Assess the morphology of the red blood cells.
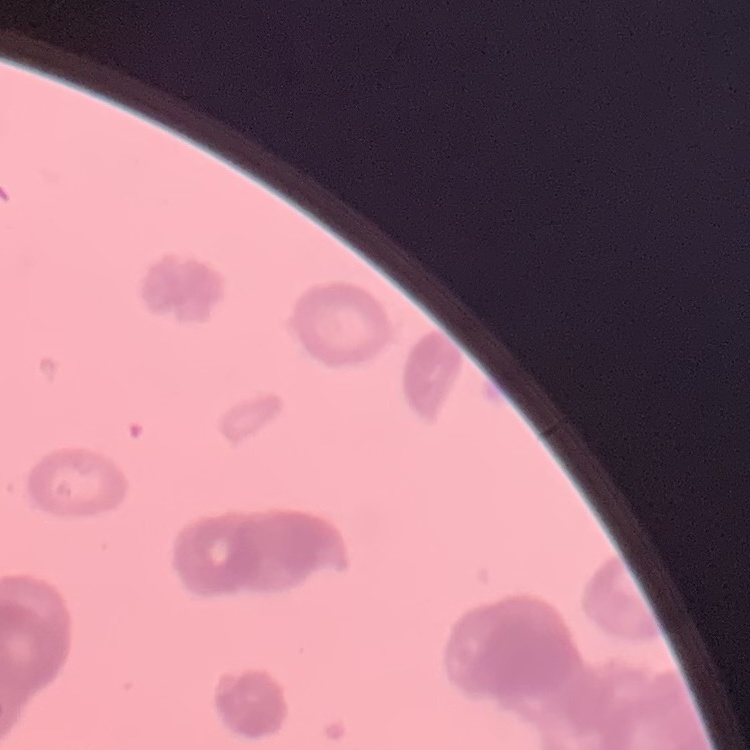
They show rouleaux formation.

Summary:
  - Image type: square crop of a larger photomicrograph
  - Preparation: thin blood film
  - Stain: Field's or Giemsa